Identify the parasite.
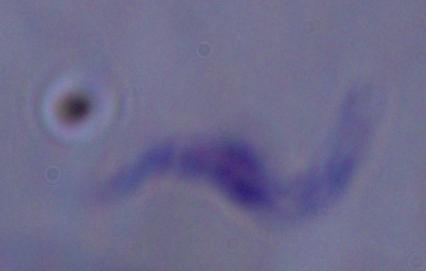
This is a trypanosome.

{
  "magnification": "1000x",
  "modality": "photomicrograph"
}